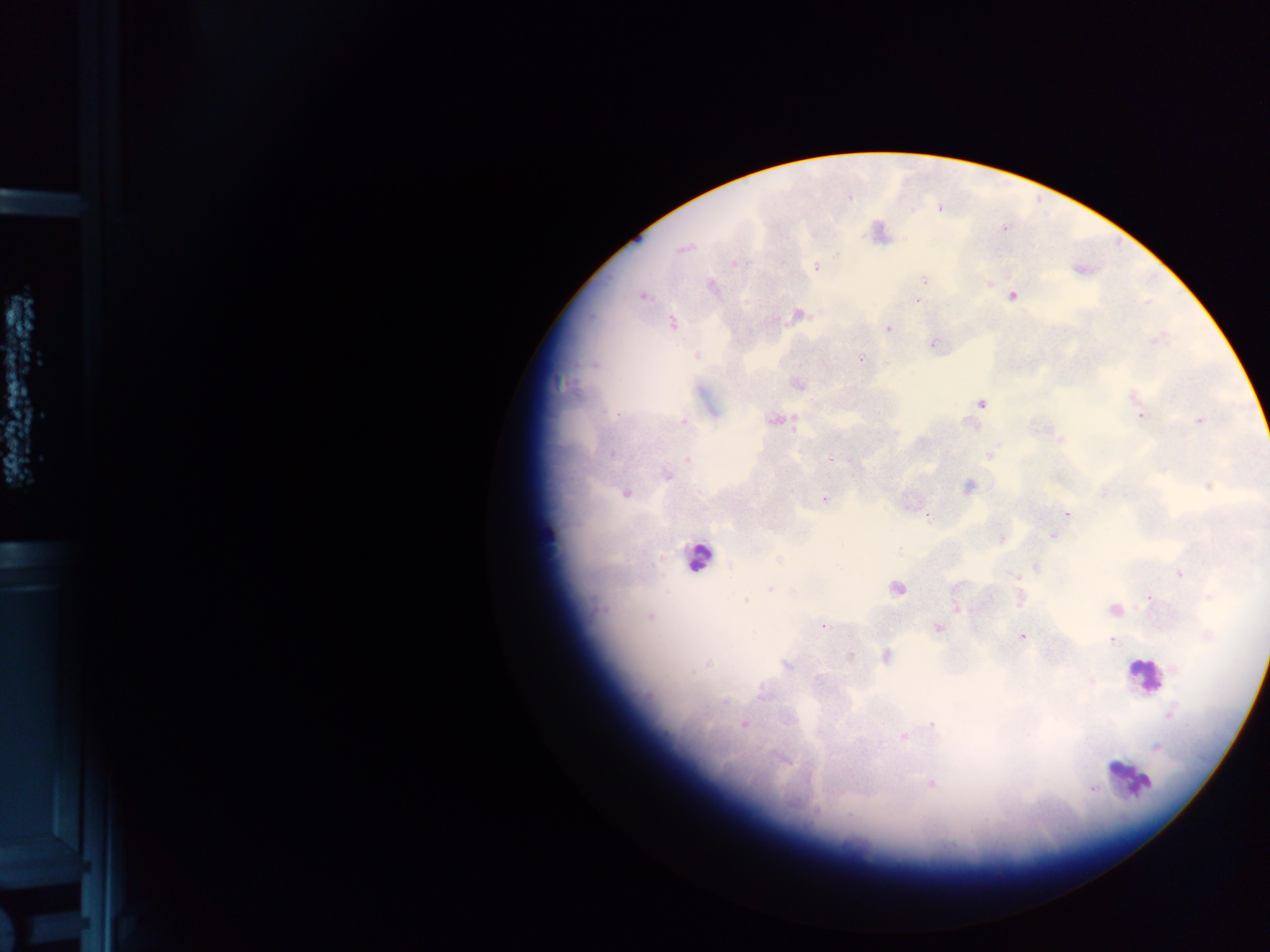

Approximate centers as [x, y] in pixels.
Summary:
  - Malaria parasite locations: [939, 208], [1004, 229], [683, 248], [836, 255], [738, 263], [817, 268], [924, 279], [990, 283], [711, 285], [642, 296], [1012, 296], [917, 301], [798, 315], [672, 323], [888, 328], [1156, 340], [933, 344], [696, 356], [861, 358], [592, 365], [798, 385], [1133, 396], [981, 404], [617, 415], [1141, 416], [774, 421], [1200, 421], [684, 422], [1060, 437], [611, 454], [989, 455], [831, 458], [687, 460], [665, 475], [968, 486], [1211, 486], [1104, 492], [626, 494], [825, 499], [1067, 514], [927, 516], [1053, 536], [1001, 539], [756, 549], [898, 550], [778, 559], [730, 566], [1035, 568], [1180, 574], [1015, 575], [770, 589], [896, 589], [1210, 596], [990, 598], [1020, 598], [1149, 598], [745, 601], [597, 609], [958, 609], [1114, 610], [649, 617], [823, 626], [937, 627], [1207, 636], [1022, 637], [1112, 641], [851, 657], [886, 657], [708, 665], [787, 666], [1176, 669], [818, 678], [1092, 682], [725, 701], [1170, 714], [743, 724], [932, 725], [904, 737], [1156, 748], [931, 784], [1090, 787]
  - Leukocyte locations: [548, 534], [696, 557], [1144, 677], [1129, 777]
  - Country: Ghana
  - Preparation: thick blood smear
  - Field of view: single
  - Image size: 1270×952 pixels
  - Capture: mobile-phone photograph through a microscope